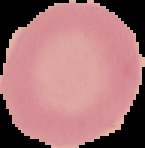

preparation = thin blood smear
image size = 145×148 pixels
image type = segmented cell region on a black background
result = negative for Plasmodium parasites